Give the position of every malaria parasite.
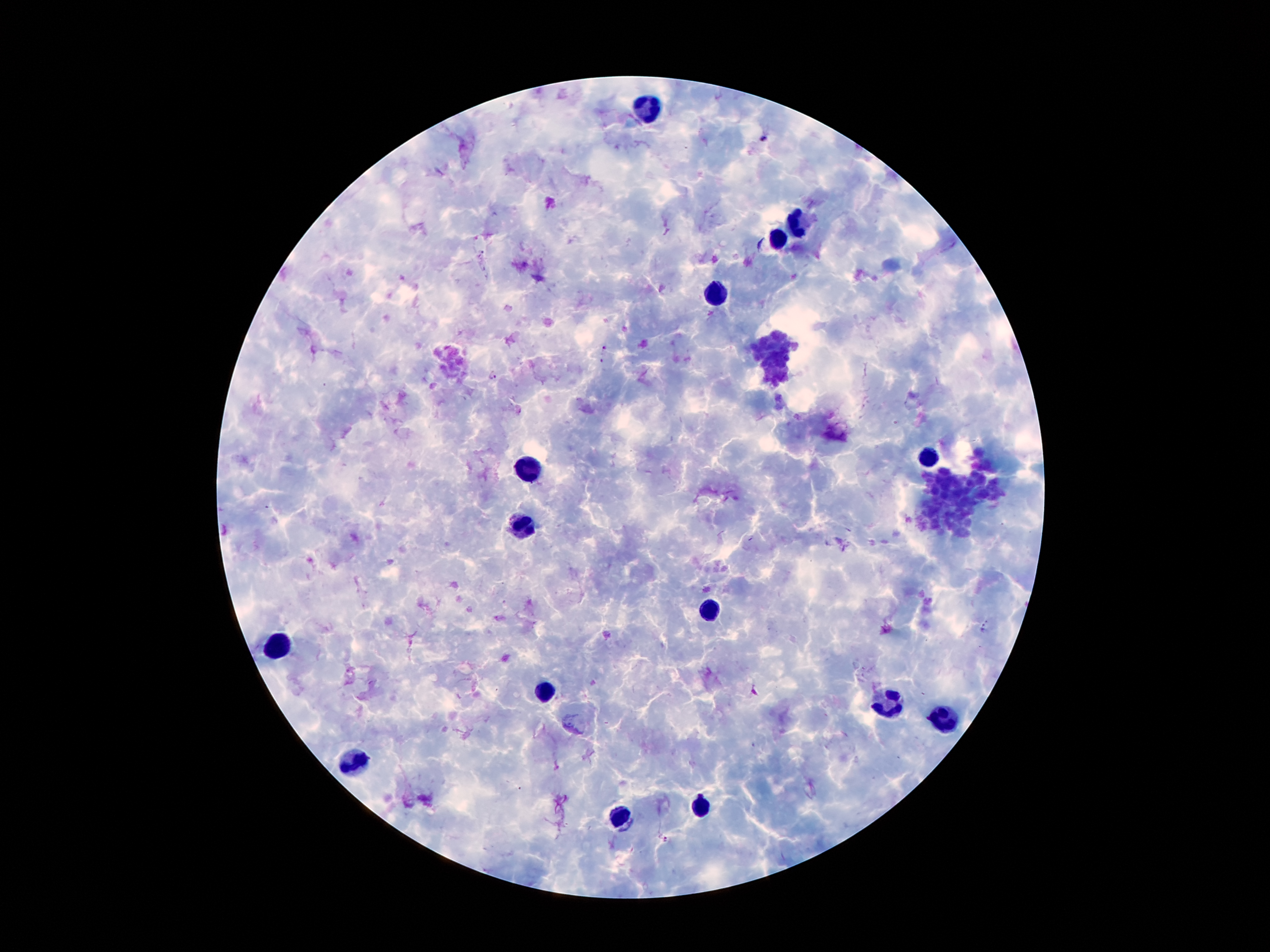
Approximate object centers, in pixels from the top-left corner.
Malaria parasites: (x=761, y=137), (x=603, y=348), (x=491, y=376), (x=984, y=627), (x=666, y=839).

Summary:
  - Leukocyte locations: (x=651, y=109), (x=794, y=221), (x=778, y=241), (x=710, y=293), (x=930, y=463), (x=530, y=468), (x=522, y=525), (x=712, y=607), (x=283, y=643), (x=549, y=691), (x=889, y=706), (x=941, y=720), (x=358, y=763), (x=703, y=807), (x=615, y=818)
  - Image size: 1270×952 pixels
  - Magnification: 100x
  - Field of view: one from this slide
  - Capture: smartphone camera through the microscope eyepiece
  - Preparation: thick peripheral-blood smear
  - Patient malaria status: positive for Plasmodium falciparum
  - Stain: Giemsa